Report the malaria status.
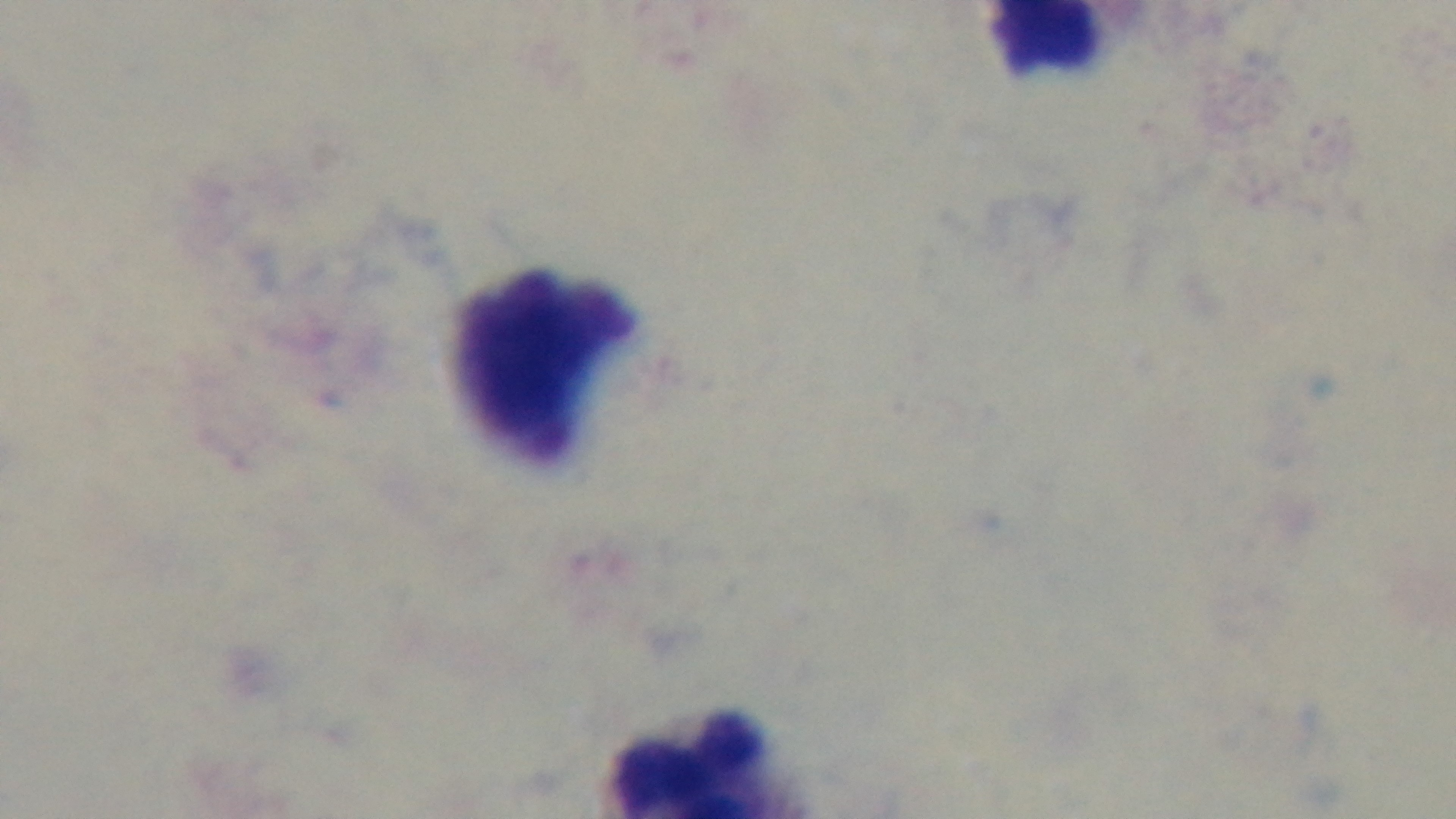

Negative.

capture: mounted 4K digital camera
objective: 100x oil immersion
modality: light microscopy
field_of_view: one from the slide
stain: Giemsa
preparation: thick